Describe the morphology of the erythrocytes.
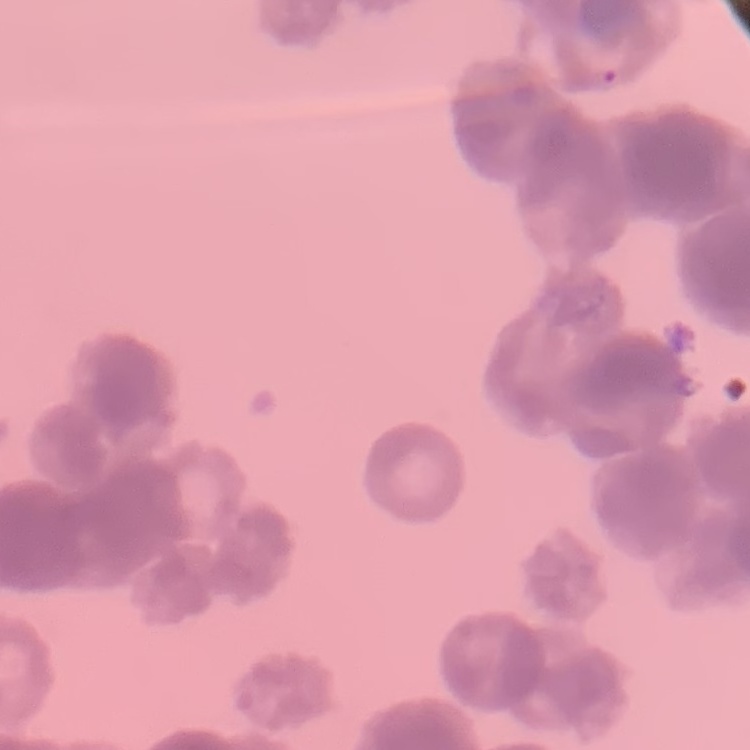

Rouleaux formation.

Summary:
  - Preparation: thin peripheral smear
  - Stain: Field's or Giemsa
  - Image type: square crop of a larger photomicrograph